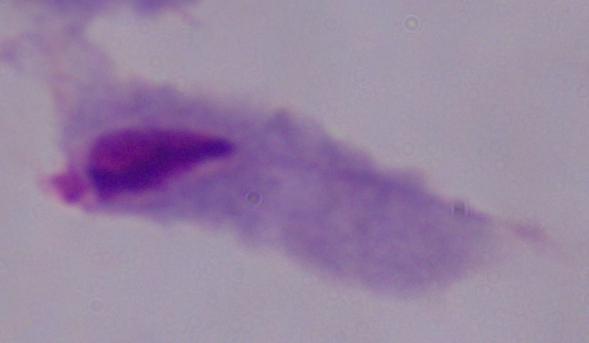

A trichomonad is shown. Micrograph. Captured at 1000x magnification.